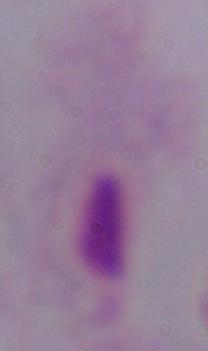
magnification = 1000x
identification = trichomonad
modality = micrograph